Assess this cell for malaria.
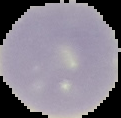
It is uninfected.

Segmented cell region on a black background. From a thin blood smear. Image is 121×118 pixels.